State which parasite is depicted.
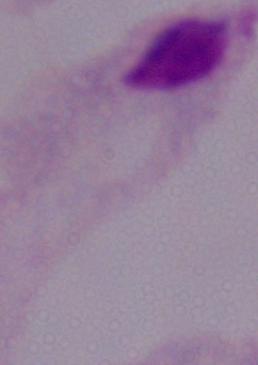
This is a trichomonad.

Photomicrograph. Captured at 1000x magnification.